Assess the morphology of the red blood cells.
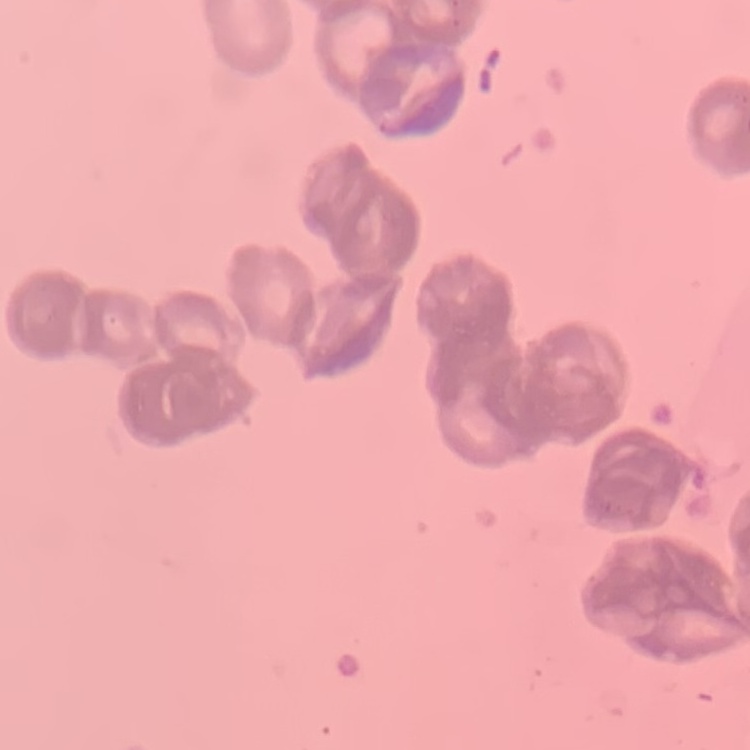

They show rouleaux formation.

{
  "preparation": "thin peripheral smear",
  "image_type": "square crop of a larger photomicrograph",
  "stain": "Field's or Giemsa"
}